Give the position of every Plasmodium parasite.
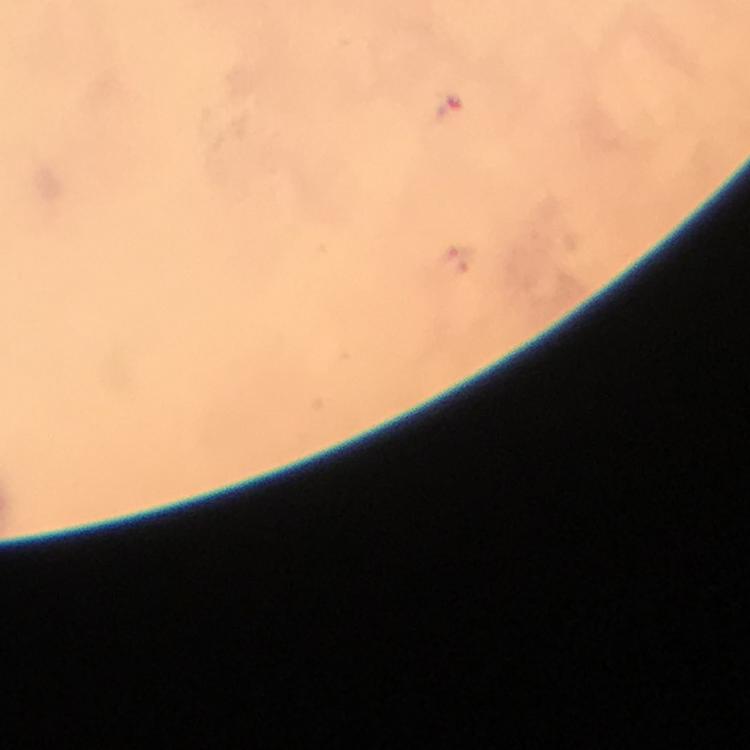

Approximate object centers, in pixels from the top-left corner.
Plasmodium parasites: (x=449, y=107).

image_size: 750×750 pixels
capture: smartphone mounted on the microscope
context: from a diagnostic examination for malaria
stain: Giemsa
preparation: thick blood film
immersion_oil: applied
magnification: 100x
cropped_from: one field of view